Assess the morphology of the erythrocytes.
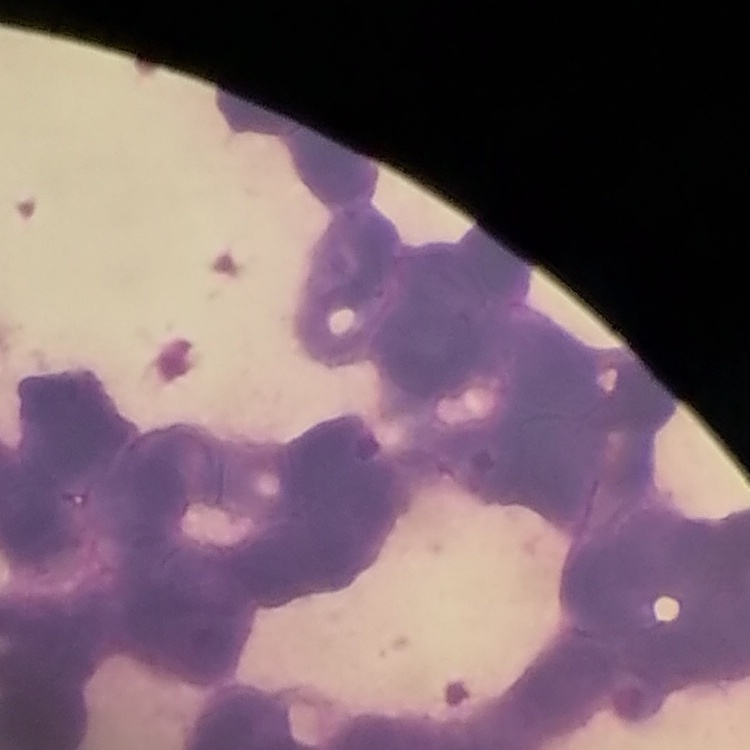

They show rouleaux formation.

stain: Field's or Giemsa
image_type: one tile cut from a larger photomicrograph
preparation: thin blood film